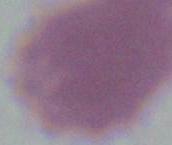

An erythrocyte is shown. Micrograph. Captured at 1000x magnification.